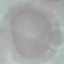
result = no malaria parasites detected
capture = smartphone camera at the microscope eyepiece
image type = automatically extracted cell patch, resized to 64 × 64 pixels
stain = Giemsa
preparation = thin smear